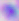 Captured at 400x magnification. Photomicrograph. Toxoplasma gondii is seen.